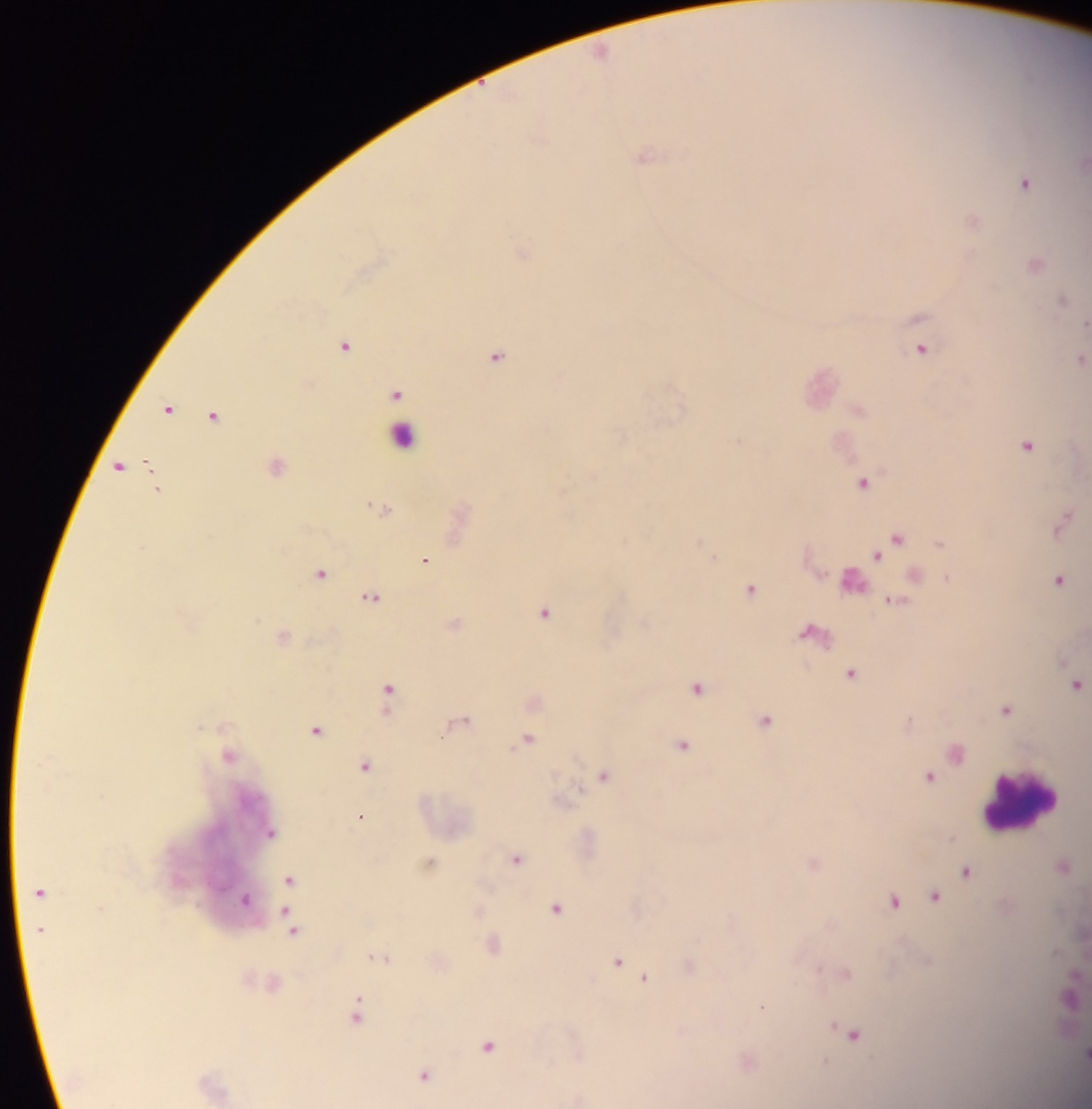 Approximate centers as (x, y) in pixels. Malaria parasite locations: (1027, 181), (971, 253), (1062, 299), (345, 344), (923, 349), (498, 356), (399, 394), (683, 406), (170, 408), (215, 415), (740, 440), (1027, 445), (121, 465), (862, 482), (899, 537), (701, 541), (942, 543), (141, 547), (877, 554), (715, 557), (427, 559), (321, 572), (1060, 579), (752, 589), (371, 597), (544, 613), (852, 672), (697, 689), (389, 690), (1006, 711), (766, 720), (912, 720), (317, 731), (530, 738), (683, 745), (366, 767), (605, 775), (929, 777), (361, 816), (290, 879), (936, 896), (895, 900), (557, 908), (286, 909), (295, 932), (619, 962), (820, 968), (845, 972), (646, 977), (359, 998), (763, 1007), (357, 1016), (834, 1025), (854, 1035), (489, 1046), (826, 1060), (425, 1074). Leukocyte locations: (396, 435), (853, 586), (1022, 810). Thick blood smear. One field of view. Image is 1092×1109 pixels. Photographed through a microscope with a mobile-phone camera. Sample from Ghana.